Evaluate for malaria.
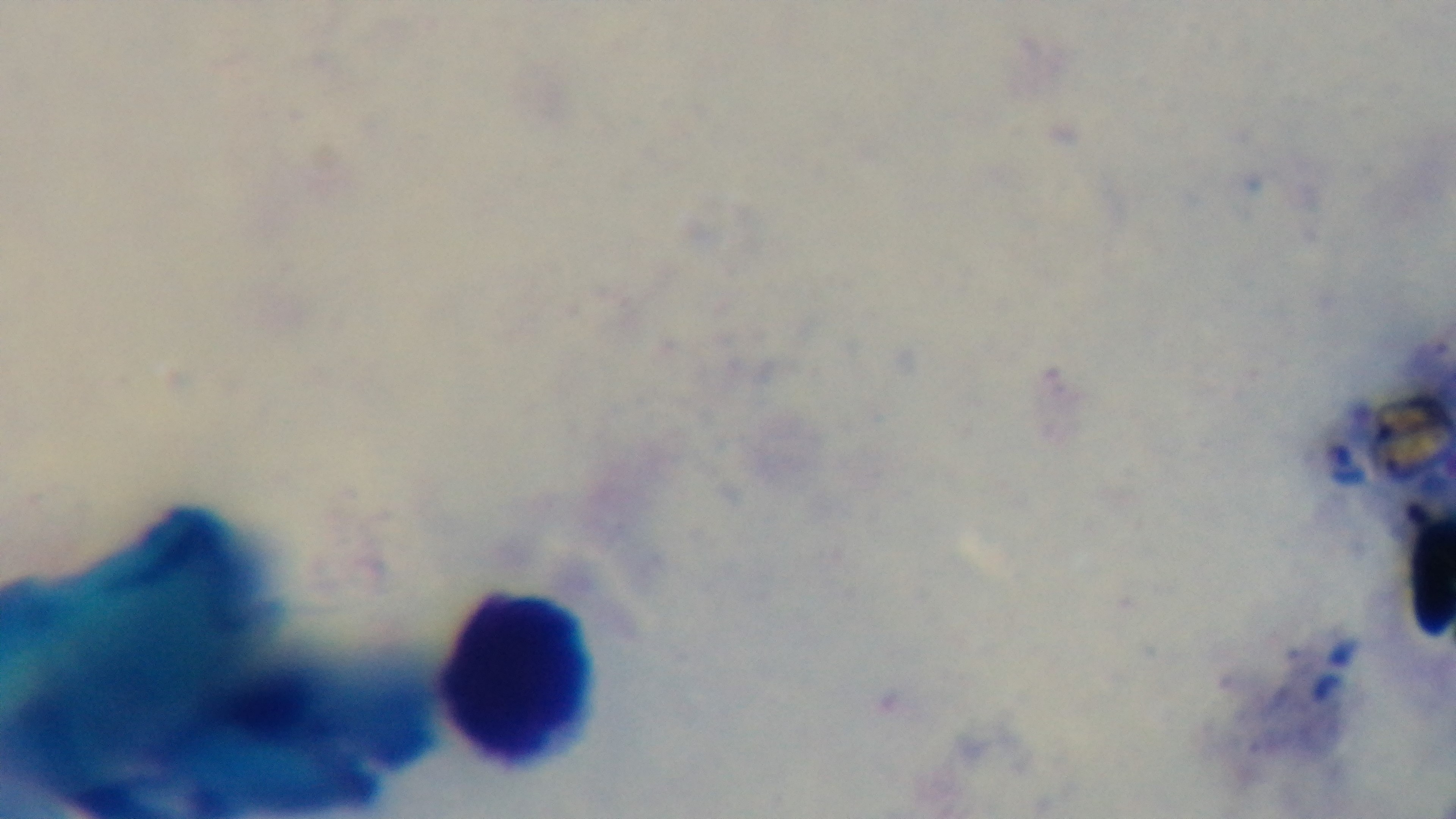

Negative.

One field from the slide. Photomicrograph. Preparation: thick blood film. 100x oil-immersion objective. Giemsa-stained. Mounted 4K digital camera.